Identify the cell.
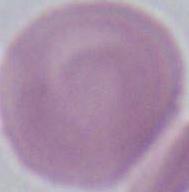
An erythrocyte.

Photomicrograph. Captured at 1000x magnification.